Locate every Plasmodium falciparum-infected red blood cell.
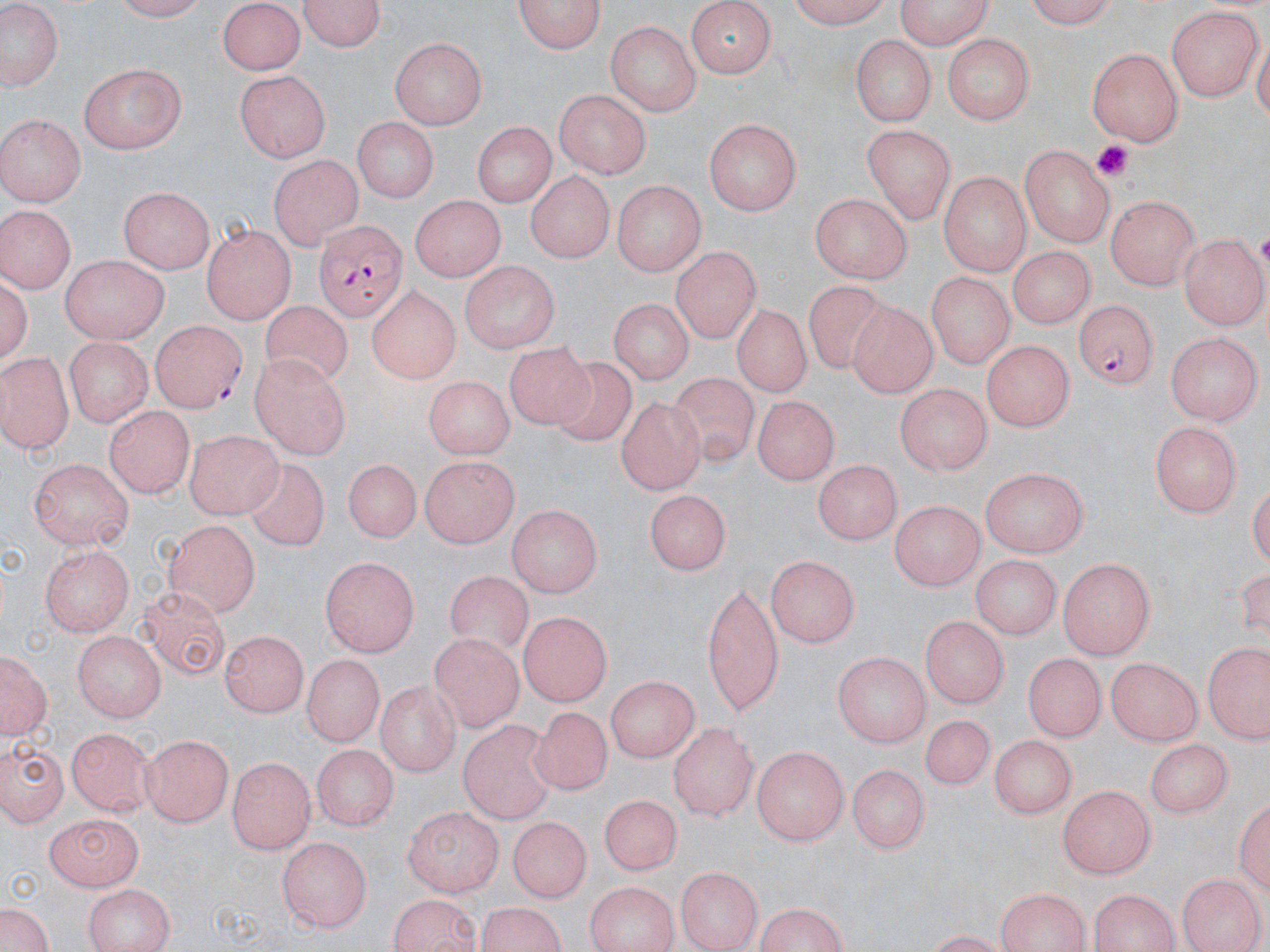

Approximate bounding boxes as [x1, y1, x2, y2] in pixels.
Plasmodium falciparum-infected red blood cells: [312, 222, 409, 316], [1073, 298, 1160, 390], [149, 320, 244, 412].

Summary:
  - Uninfected red blood cell locations: [109, 0, 219, 21], [296, 0, 387, 52], [778, 0, 892, 27], [892, 0, 996, 48], [1018, 0, 1120, 26], [216, 2, 307, 75], [513, 2, 608, 54], [0, 3, 65, 92], [685, 4, 777, 76], [1164, 6, 1260, 100], [606, 19, 699, 116], [389, 35, 486, 126], [848, 35, 938, 126], [940, 35, 1036, 123], [1087, 48, 1184, 144], [80, 63, 185, 155], [234, 69, 332, 163], [554, 89, 651, 178], [0, 115, 85, 206], [355, 117, 438, 201], [705, 117, 801, 218], [473, 121, 554, 209], [861, 125, 955, 221], [1021, 146, 1114, 248], [270, 156, 361, 248], [525, 168, 615, 265], [940, 168, 1029, 276], [612, 177, 706, 275], [118, 186, 211, 271], [407, 194, 509, 278], [806, 194, 915, 281], [1104, 195, 1196, 288], [0, 202, 76, 294], [201, 221, 296, 323], [1181, 234, 1267, 326], [672, 244, 761, 345], [1007, 247, 1096, 328], [61, 254, 168, 344], [456, 261, 561, 355], [927, 271, 1012, 367], [802, 282, 892, 370], [362, 286, 459, 384], [614, 294, 699, 379], [848, 297, 938, 398], [258, 299, 355, 391], [731, 304, 808, 398], [1167, 331, 1262, 426], [63, 339, 152, 428], [984, 339, 1073, 431], [503, 340, 602, 440], [0, 350, 72, 451], [249, 354, 353, 461], [551, 356, 638, 448], [672, 372, 769, 466], [420, 375, 515, 459], [894, 383, 993, 473], [750, 393, 840, 479], [616, 397, 707, 491], [103, 405, 197, 498], [1151, 421, 1244, 514], [187, 428, 280, 519], [419, 452, 518, 547], [29, 458, 134, 550], [242, 458, 327, 554], [339, 459, 421, 549], [810, 460, 899, 544], [982, 467, 1090, 558], [646, 488, 732, 570], [894, 499, 985, 592], [508, 505, 600, 600], [164, 518, 259, 619], [39, 541, 135, 632], [972, 550, 1058, 635], [769, 555, 862, 644], [320, 557, 420, 657], [1059, 558, 1155, 658], [445, 569, 534, 653], [699, 579, 786, 715], [139, 586, 231, 683], [518, 611, 611, 707], [921, 615, 1005, 710], [73, 629, 165, 723], [220, 630, 305, 716], [431, 632, 526, 728], [1201, 639, 1270, 746], [0, 648, 50, 745], [830, 648, 934, 744], [1025, 650, 1106, 738], [299, 654, 381, 745], [1106, 659, 1202, 747], [608, 675, 700, 763], [376, 679, 464, 777], [520, 705, 620, 798], [918, 714, 995, 793], [452, 722, 560, 823], [671, 722, 756, 819], [68, 729, 154, 816], [141, 734, 234, 827], [991, 734, 1079, 821], [2, 736, 71, 825], [1145, 738, 1236, 823], [313, 741, 397, 829], [753, 746, 848, 845], [227, 754, 315, 855], [849, 761, 931, 853], [1056, 786, 1154, 877], [598, 793, 677, 876], [403, 809, 502, 897], [44, 814, 145, 889], [505, 816, 588, 903], [277, 836, 370, 934], [675, 865, 762, 949], [1178, 872, 1266, 952], [583, 881, 682, 952], [82, 882, 174, 952], [994, 887, 1092, 952], [1088, 890, 1181, 952], [385, 892, 484, 951], [750, 900, 851, 952], [473, 902, 574, 952], [1, 908, 50, 952]
  - Platelet locations: [1090, 139, 1139, 182]
  - Slide-level diagnosis: Plasmodium falciparum
  - Image size: 1270×952 pixels
  - Preparation: thin blood smear
  - Field of view: single
  - Magnification: 1000x
  - Stain: May-Grünwald-Giemsa
  - Modality: optical microscopy